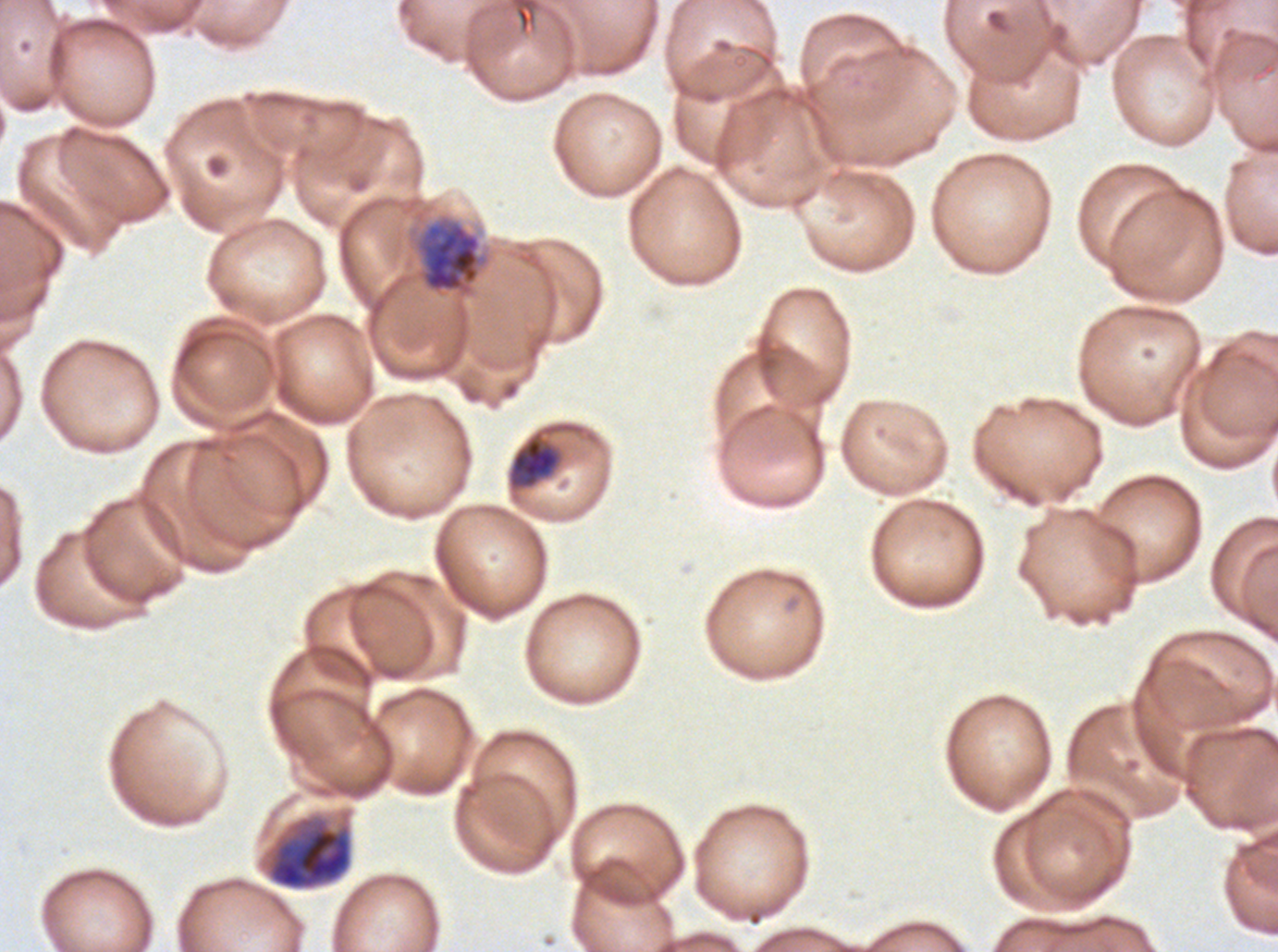
late_ring_early_trophozoite_locations: 'approximate bounding boxes as (x1, y1, x2, y2) in pixels: (506, 421, 582, 493)'
early_schizont_locations: 'approximate bounding boxes as (x1, y1, x2, y2) in pixels: (412, 214, 490, 299)'
late_schizont_locations: 'approximate bounding boxes as (x1, y1, x2, y2) in pixels: (266, 815, 352, 890)'
specimen: P. falciparum from a patient in The Gambia, cultured ex vivo for 24 to 48 hours
field_of_view: one sub-image of a larger composite
preparation: thin blood smear
stain: Giemsa
image_size: 1278×952 pixels
life_cycle_stages_observed: late-ring/early-trophozoite, early schizont, late schizont